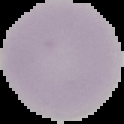 From a thin blood film. Image is 124×124 pixels. The area outside the segmented cell region is set to black. Result: no malaria parasites seen.